Assess this cell for malaria.
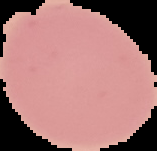
It is uninfected.

{
  "preparation": "thin blood film",
  "image_size": "157×151 pixels",
  "image_type": "cell region segmented out of the field of view; surrounding area masked to black"
}